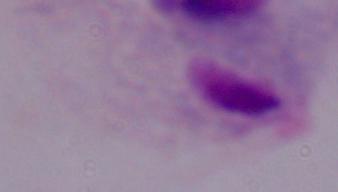

identification: trichomonad
modality: micrograph
magnification: 1000x